Report the malaria status.
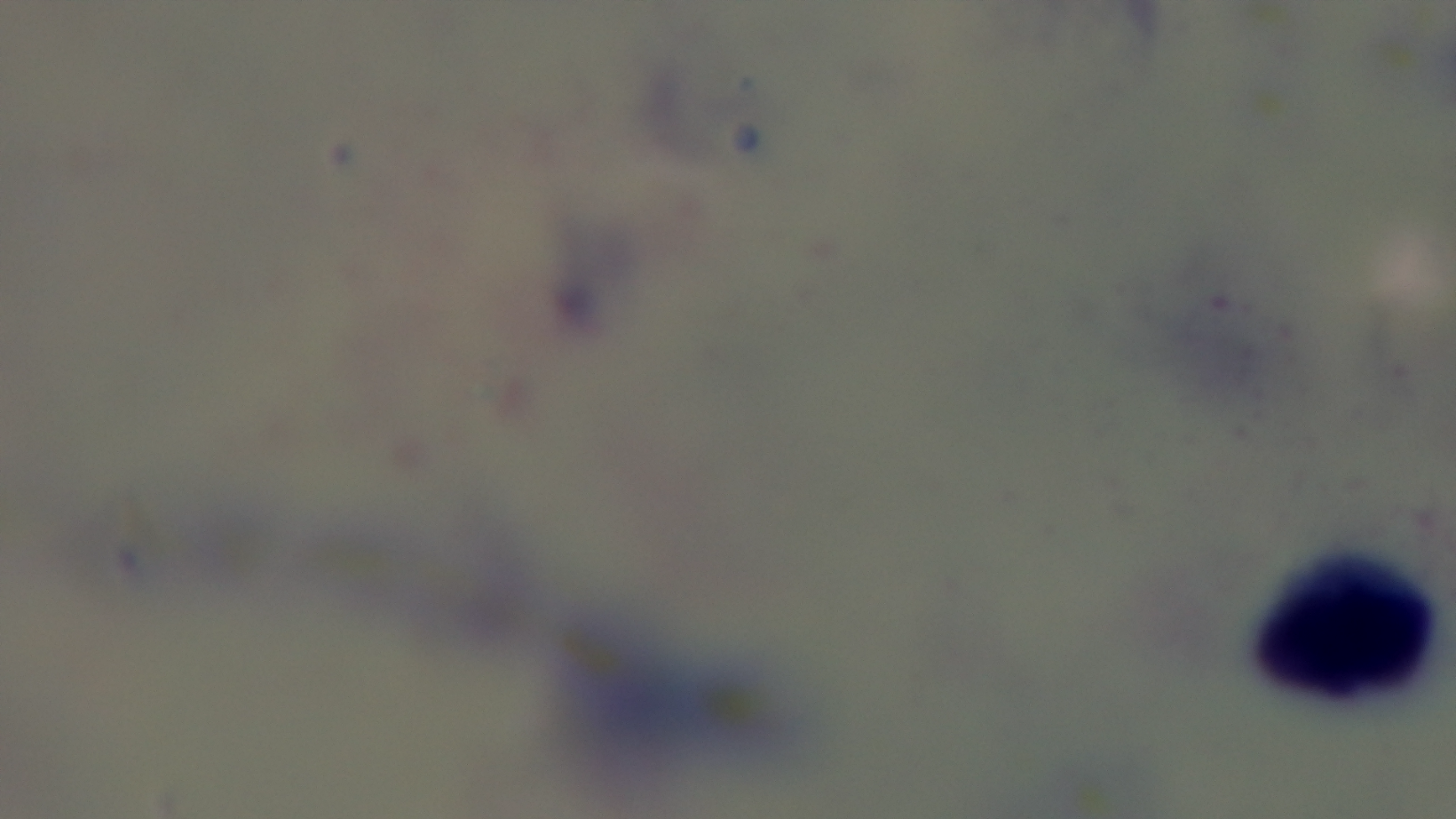
Uninfected.

100x oil-immersion objective. One field from the slide. Preparation: thick blood film. Photomicrograph. Mounted 4K digital camera. Giemsa stain.